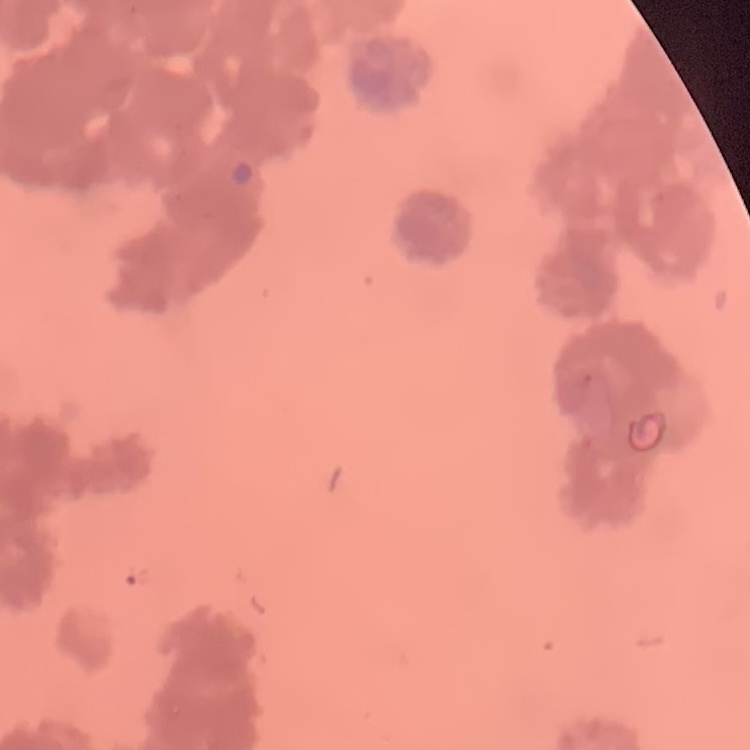 The red blood cells exhibit rouleaux formation. Square crop of a larger photomicrograph. Field's or Giemsa stain. Thin blood film.